Outline each uninfected red blood cell.
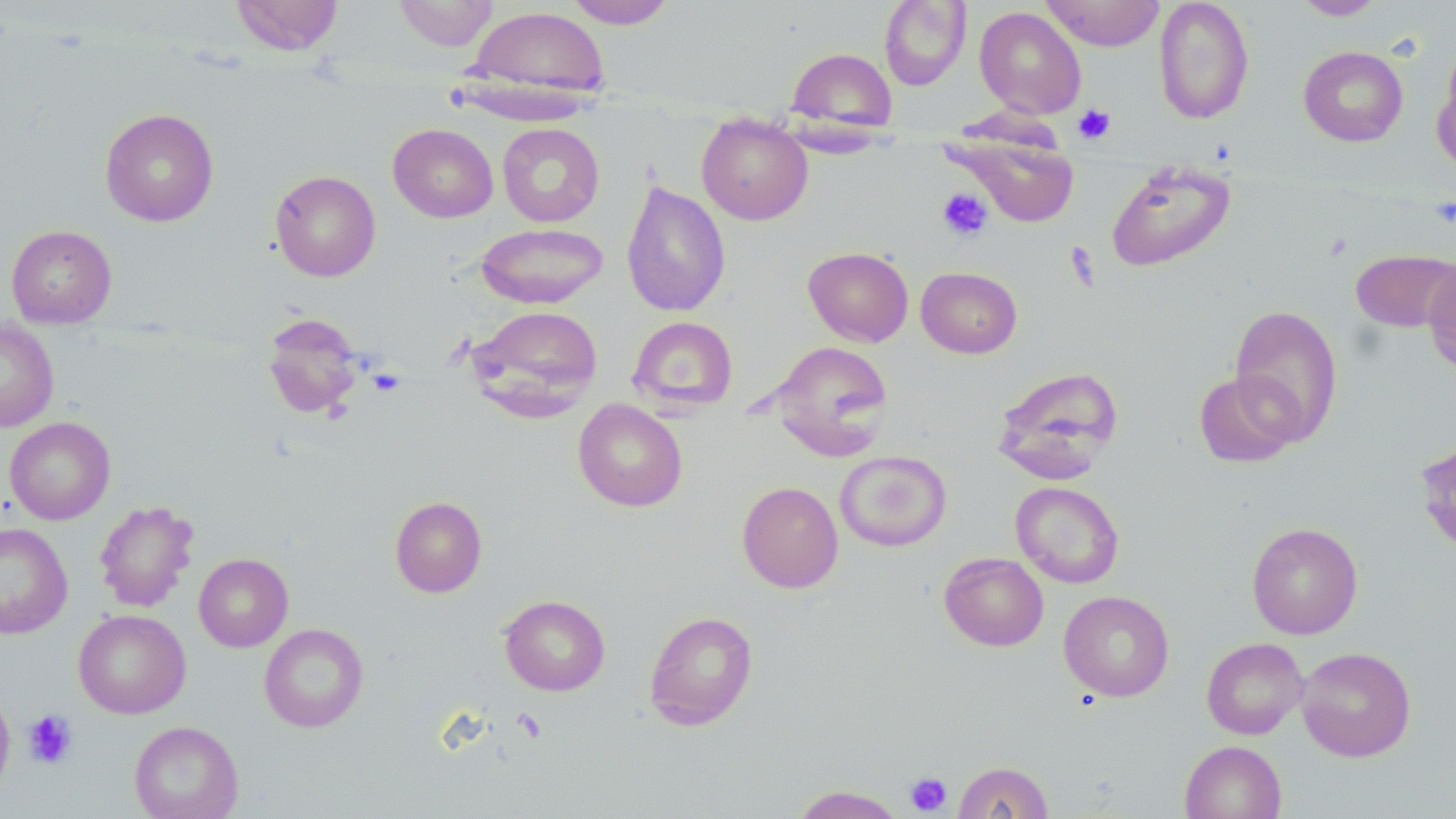
Approximate bounding boxes as (x1,y1)-(x2,y2) corner pairs in pixels.
Uninfected red blood cells: (231,0)-(344,55), (393,0)-(499,51), (563,0)-(677,29), (1041,0)-(1165,51), (1153,0)-(1255,124), (1293,0)-(1385,21), (879,1)-(971,90), (466,5)-(611,101), (974,6)-(1086,119), (1298,45)-(1408,147), (786,47)-(897,134), (1433,56)-(1456,173), (99,108)-(219,226), (696,114)-(813,226), (388,123)-(498,223), (497,123)-(605,227), (947,134)-(1082,227), (1106,160)-(1235,272), (270,170)-(381,281), (621,180)-(731,318), (475,223)-(609,309), (6,225)-(117,327), (803,246)-(914,347), (1351,249)-(1455,332), (1423,255)-(1456,376), (916,266)-(1022,358), (1229,303)-(1344,446), (469,305)-(603,417), (261,313)-(366,420), (628,316)-(738,414), (0,318)-(59,432), (767,341)-(893,459), (992,366)-(1124,483), (1193,370)-(1303,468), (573,398)-(688,512), (4,417)-(116,524), (1415,433)-(1456,560), (835,450)-(952,551), (737,481)-(843,593), (1010,481)-(1124,588), (389,496)-(488,597), (94,500)-(199,612), (1247,522)-(1363,639), (0,523)-(73,638), (939,552)-(1048,651), (193,553)-(293,652), (1058,590)-(1174,702), (499,594)-(610,696), (73,609)-(191,718), (644,610)-(759,731), (259,623)-(368,733), (1201,637)-(1308,740), (1296,646)-(1416,761), (0,686)-(15,797), (129,720)-(244,819), (1180,741)-(1287,819), (952,761)-(1054,819), (790,785)-(908,818).

Platelet locations: (1073,104)-(1116,144), (936,187)-(993,241), (1429,197)-(1456,228), (367,368)-(406,397), (511,707)-(546,742), (22,709)-(78,769), (905,772)-(952,815). Slide-level diagnosis: no evidence of blood parasites. Single field of view. Captured at 1000x magnification. Optical microscopy. May-Grünwald-Giemsa-stained preparation. Image is 1456×819 pixels. Thin blood smear.